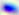

magnification = 400x
modality = photomicrograph
identification = Toxoplasma gondii